Report the malaria status of this cell.
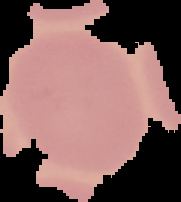

It is uninfected.

{
  "image_type": "segmented cell region on a black background",
  "preparation": "thin blood smear",
  "image_size": "181×202 pixels"
}